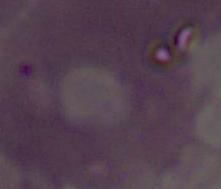

modality: photomicrograph
identification: red blood cell
magnification: 1000x